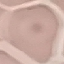

Malaria status: uninfected. Cell patch, automatically extracted from a larger field of view and resized to 64 × 64 pixels. Thin blood film. Acquired by smartphone through the microscope eyepiece. Giemsa stain.